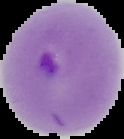

From a thin blood smear. Cell region segmented out of the field of view; the surrounding area is masked to black. Image is 124×139 pixels. Result: Plasmodium parasites identified.